Point out each Plasmodium parasite.
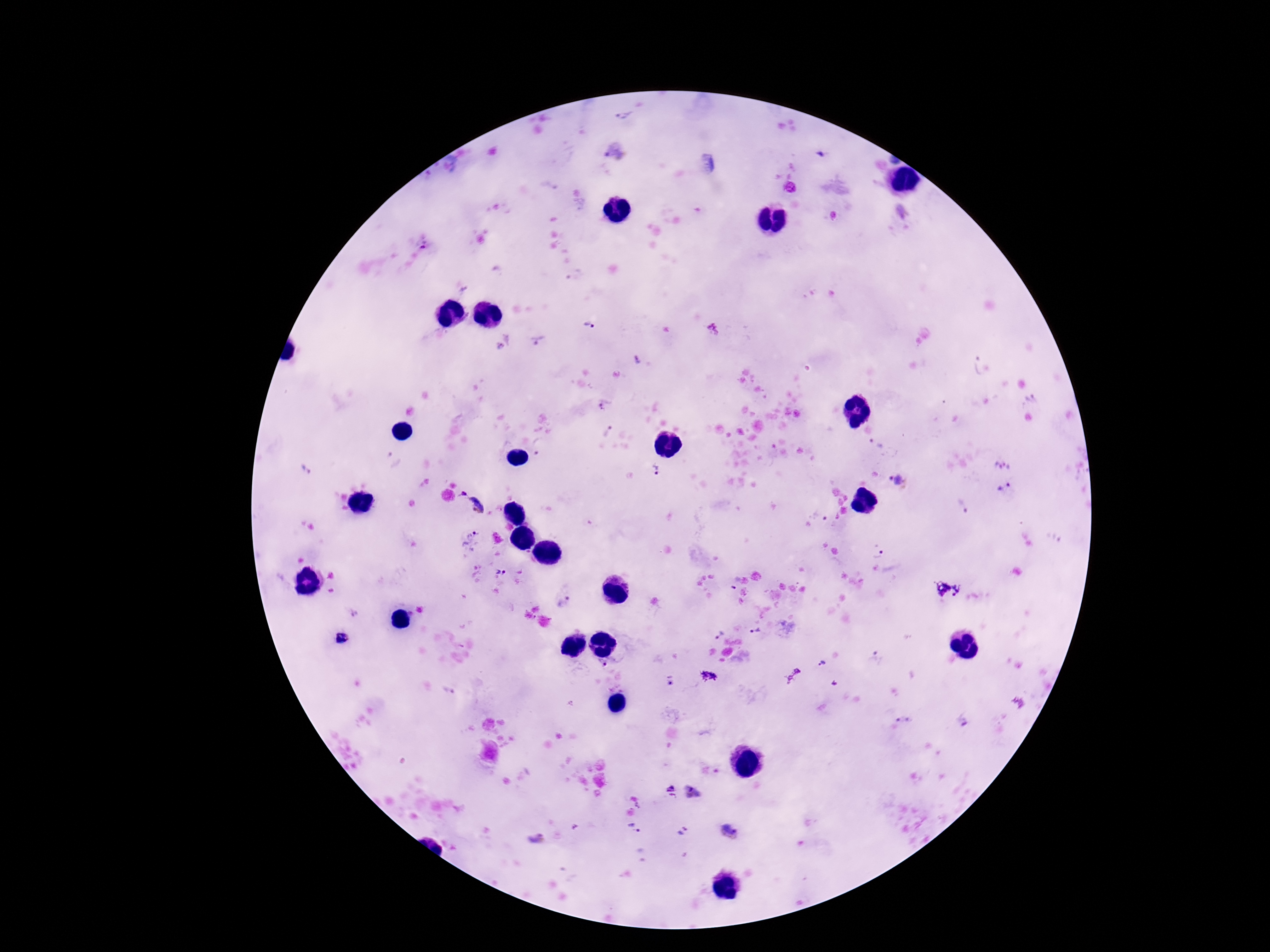

Approximate centers as [x, y] in pixels.
Plasmodium parasites: [626, 116], [615, 152], [790, 188], [902, 210], [422, 248], [589, 325], [713, 328], [538, 340], [638, 360], [972, 366], [1032, 399], [604, 407], [608, 430], [876, 444], [541, 446], [773, 452], [306, 470], [656, 470], [896, 482], [1004, 488], [463, 494], [476, 505], [961, 507], [819, 515], [471, 538], [877, 554], [501, 572], [735, 583], [947, 589], [565, 602], [756, 632], [718, 634], [343, 638], [822, 663], [608, 664], [709, 675], [670, 681], [446, 691], [903, 719], [962, 719], [671, 788], [691, 792], [634, 829], [728, 830], [683, 832], [537, 838].

Smartphone photograph taken through the microscope eyepiece. 100x magnification. Giemsa stain. Single field of view. Image is 1270×952 pixels. Thick blood film. Patient malaria status: positive.